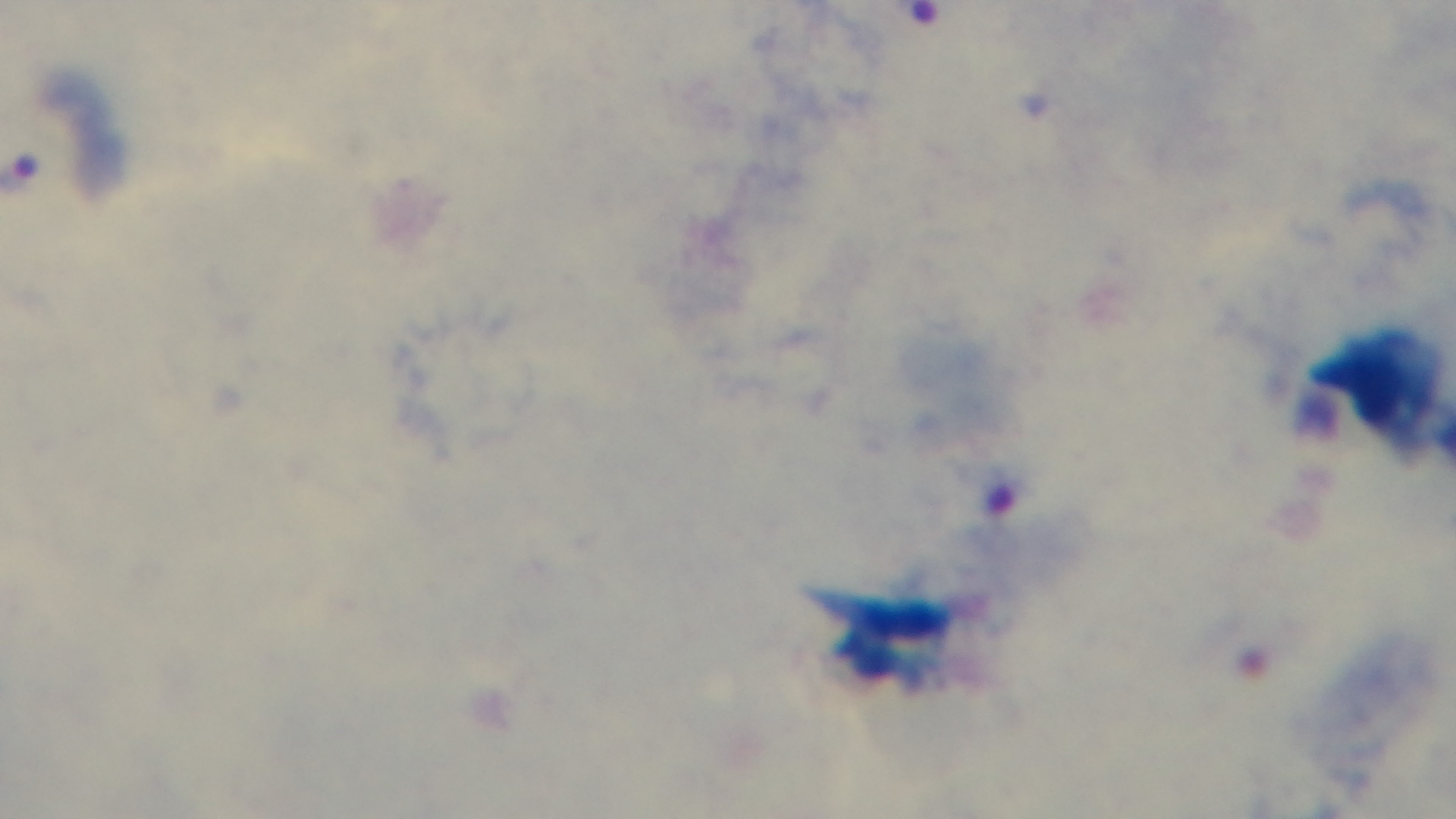

Summary:
  - Preparation: thick
  - Stain: Giemsa
  - Objective: 100x oil immersion
  - Capture: mounted 4K digital camera
  - Field of view: single
  - Modality: light microscopy
  - Malaria status: positive